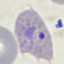

Result: malaria parasites detected. Giemsa stain. Thin blood smear. Acquired by smartphone through the microscope eyepiece. Cell patch, automatically extracted from a larger field of view and resized to 64 × 64 pixels.